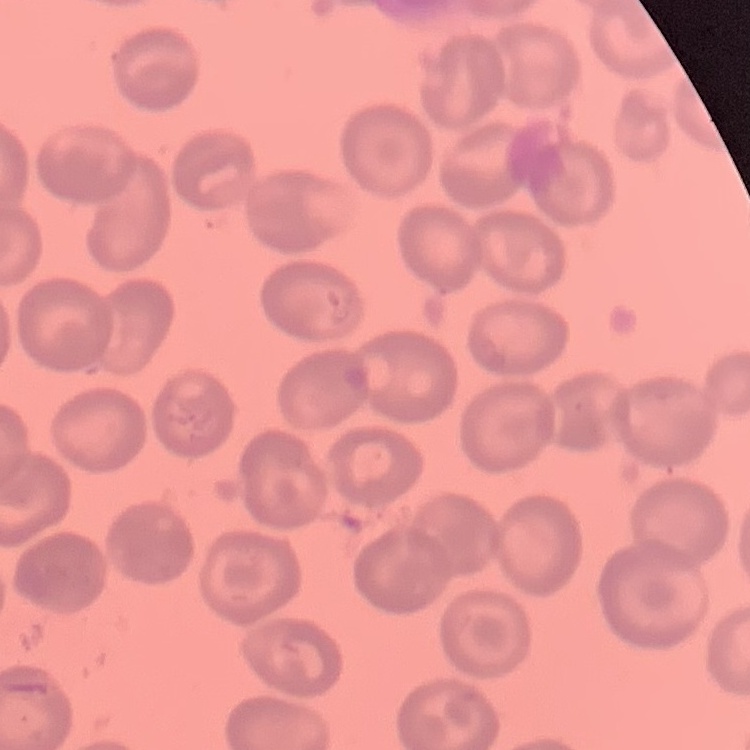

The erythrocytes exhibit no rouleaux formation. Thin blood smear. Square crop of a larger photomicrograph. Field's or Giemsa stain.